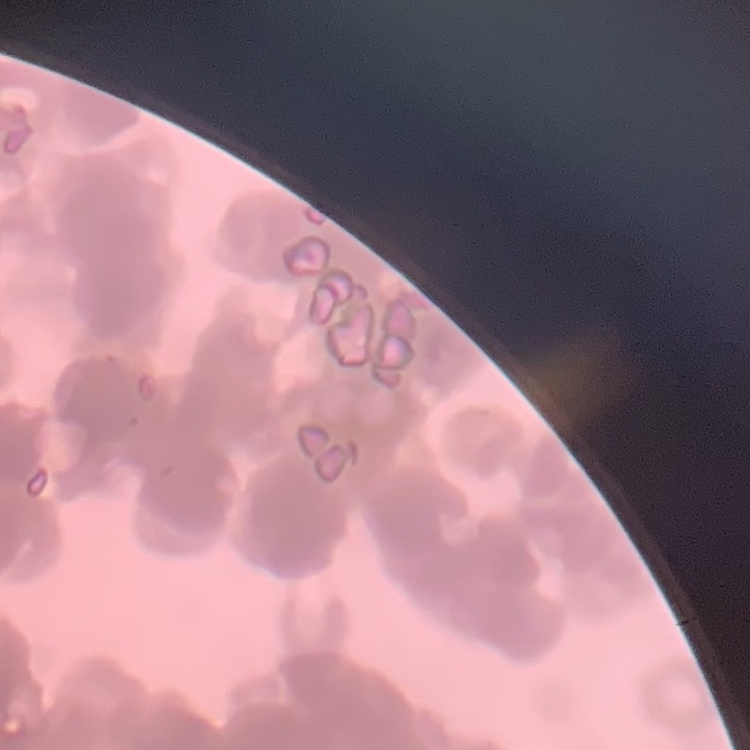
Summary:
  - Erythrocyte morphology: rouleaux formation
  - Stain: Field's or Giemsa
  - Image type: square crop of a larger photomicrograph
  - Preparation: thin peripheral smear